Assess this cell for malaria.
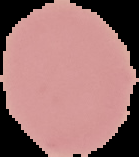

Uninfected.

The area outside the segmented cell region is set to black. From a thin blood smear. Image is 139×157 pixels.